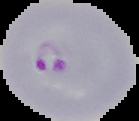
image_type: segmented cell region with the area outside set to black
result: malaria parasites detected
image_size: 139×121 pixels
preparation: thin blood film